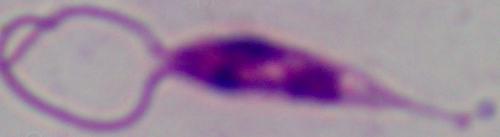

Summary:
  - Identification: Leishmania
  - Magnification: 1000x
  - Modality: photomicrograph